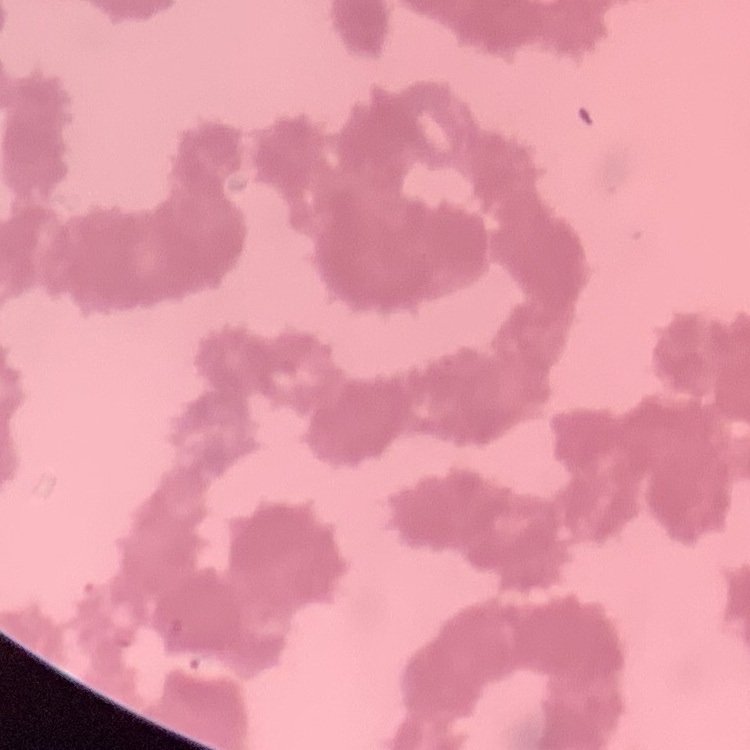
Summary:
  - Erythrocyte morphology: rouleaux formation
  - Image type: square crop of a larger photomicrograph
  - Stain: Field's or Giemsa
  - Preparation: thin blood film